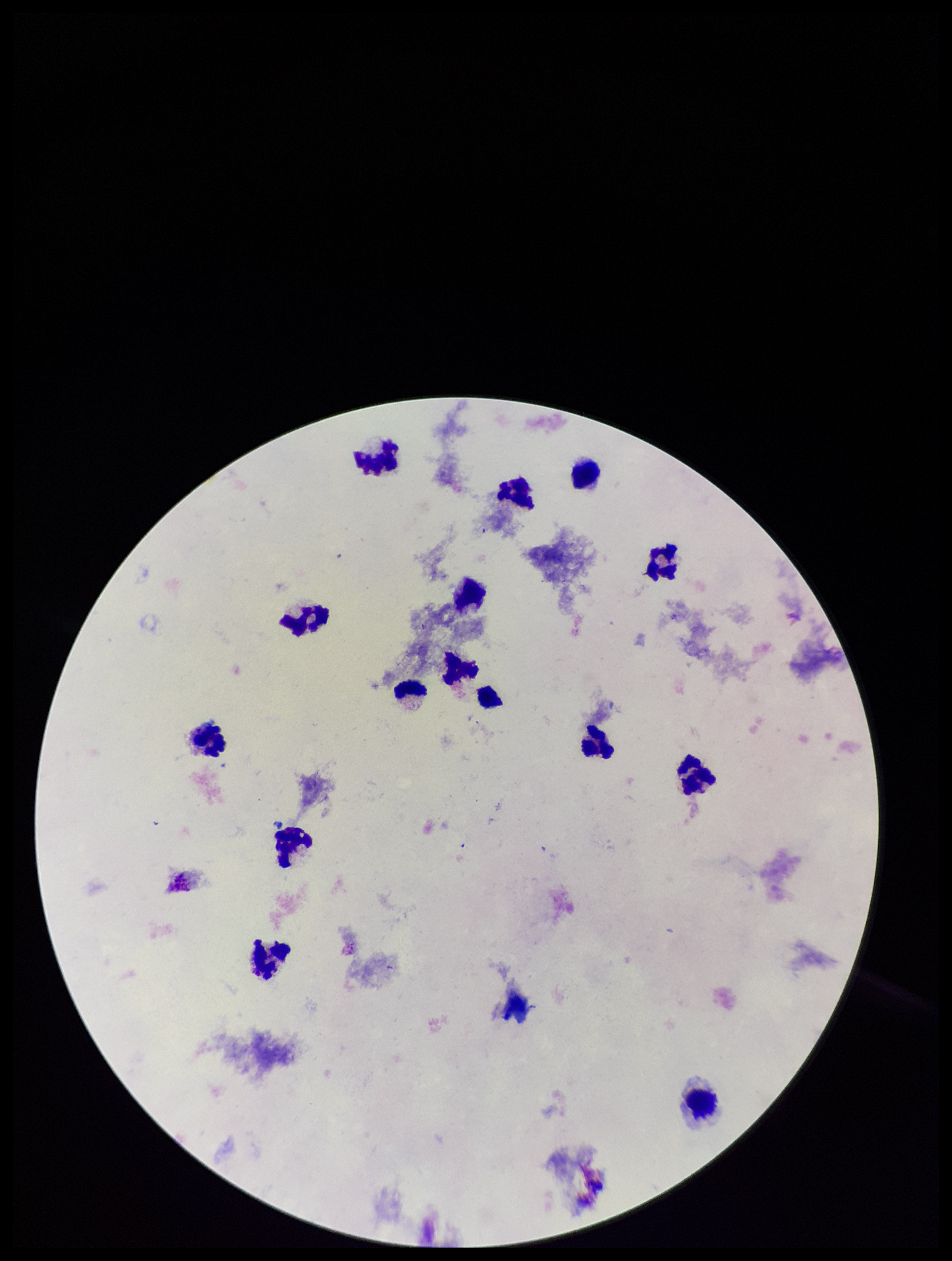 Plasmodium parasites: none detected. Parasite count: 0. Photographed through the microscope eyepiece with a smartphone camera. Image is 952×1261 pixels. Leukocyte count: 15. Single field of view. Preparation: thick smear. Stained with Giemsa. Patient malaria status: negative.